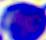 400x magnification. A white blood cell is seen. Micrograph.